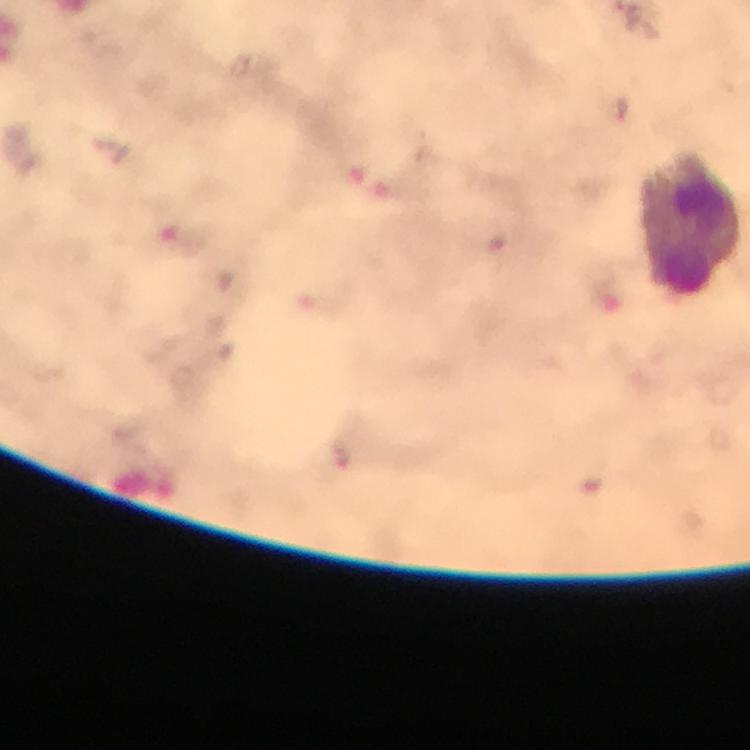

Approximate centers as {x, y} in pixels. Leukocyte locations: {691, 223}. Plasmodium parasites: none seen. At 100x magnification. Photographed through the microscope with a smartphone camera. Cropped region of a single field of view. Thick blood film. Image is 750×750 pixels. Immersion oil applied. From a diagnostic examination for malaria. Giemsa-stained preparation.